Outline each Plasmodium falciparum-infected red blood cell.
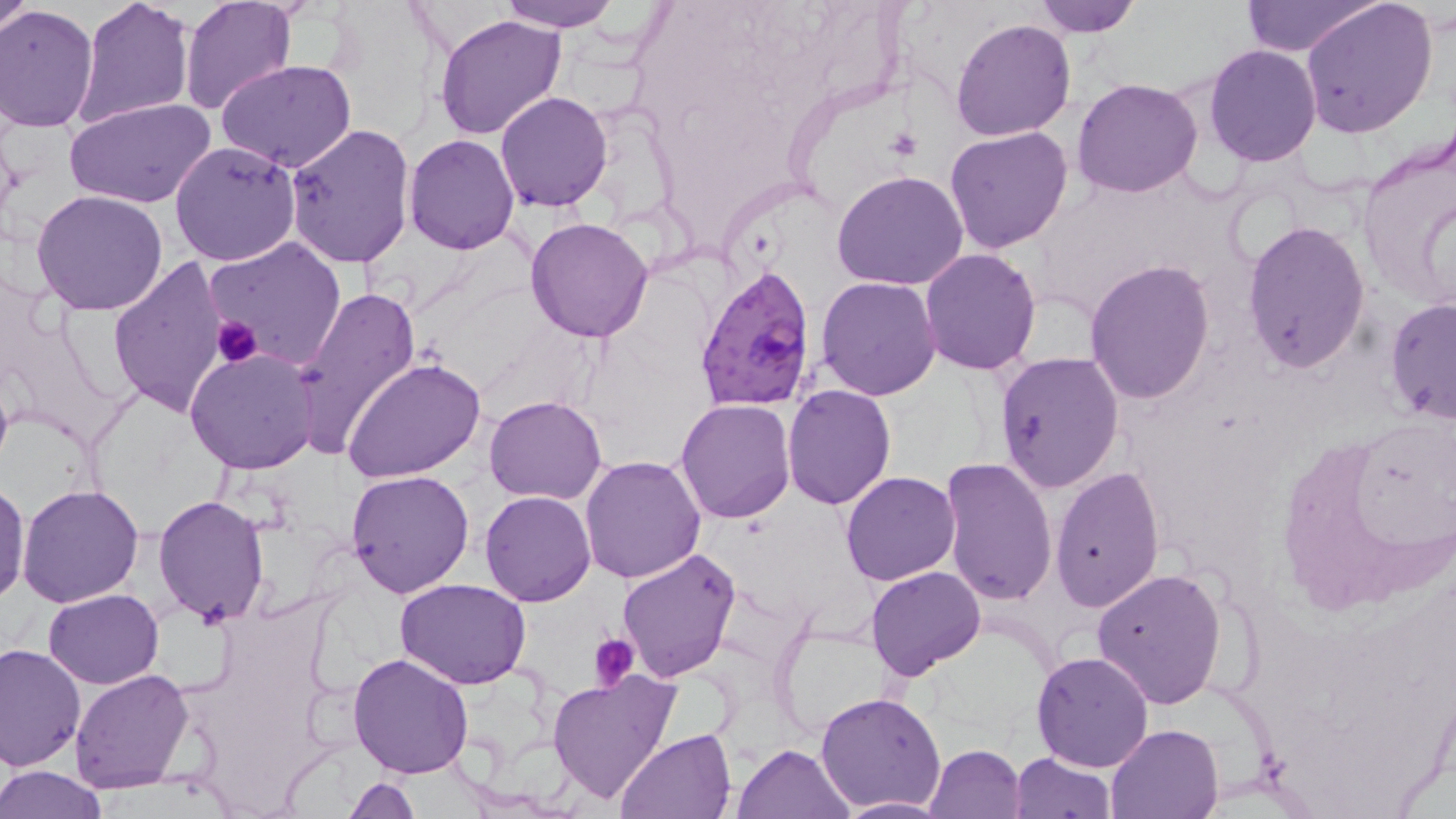

Approximate bounding boxes as [x1, y1, x2, y2] in pixels.
Plasmodium falciparum-infected red blood cells: [694, 265, 821, 414].

slide_level_diagnosis: Plasmodium falciparum
modality: light microscopy
magnification: 1000x
uninfected_red_blood_cell_locations: 'approximate bounding boxes as [x1, y1, x2, y2] in pixels: [0, 0, 33, 36], [75, 0, 195, 129], [496, 0, 621, 33], [1029, 0, 1143, 37], [1238, 0, 1378, 55], [1300, 0, 1441, 139], [180, 1, 298, 116], [0, 5, 101, 134], [433, 12, 567, 141], [950, 17, 1076, 141], [1204, 45, 1322, 166], [216, 59, 357, 172], [1072, 77, 1204, 198], [495, 90, 613, 211], [63, 96, 215, 207], [284, 124, 417, 270], [945, 126, 1073, 253], [1357, 129, 1456, 309], [404, 134, 520, 256], [170, 140, 302, 266], [830, 171, 971, 292], [30, 189, 169, 315], [526, 217, 654, 341], [1241, 220, 1370, 373], [206, 236, 347, 372], [919, 247, 1041, 375], [108, 256, 234, 418], [1086, 260, 1216, 404], [817, 277, 941, 400], [287, 284, 423, 457], [1384, 297, 1456, 426], [184, 349, 319, 474], [996, 351, 1125, 492], [344, 356, 484, 484], [782, 384, 895, 509], [484, 395, 608, 503], [676, 398, 796, 522], [580, 455, 706, 582], [939, 455, 1058, 604], [1050, 467, 1165, 612], [346, 468, 474, 597], [841, 471, 961, 585], [0, 480, 32, 606], [18, 485, 143, 607], [481, 489, 596, 605], [154, 495, 271, 625], [616, 549, 742, 683], [866, 566, 984, 680], [1093, 566, 1226, 708], [394, 579, 532, 690], [43, 588, 164, 689], [0, 643, 84, 772], [1030, 650, 1155, 772], [348, 652, 474, 777], [70, 667, 195, 793], [546, 669, 680, 804], [815, 691, 948, 812], [1104, 723, 1224, 817], [614, 728, 736, 818], [735, 743, 856, 819], [925, 743, 1026, 817], [1011, 752, 1116, 817], [0, 766, 108, 819], [344, 776, 422, 818], [834, 797, 951, 817]'
field_of_view: one of a larger specimen
stain: May-Grünwald-Giemsa
image_size: 1456×819 pixels
preparation: thin blood film
platelet_locations: 'approximate bounding boxes as [x1, y1, x2, y2] in pixels: [888, 126, 920, 157], [210, 316, 264, 369], [589, 633, 639, 689]'